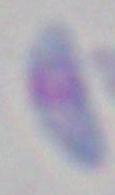

Toxoplasma gondii is seen. Captured at 1000x magnification. Photomicrograph.